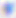
magnification: 400x
modality: photomicrograph
identification: Toxoplasma gondii